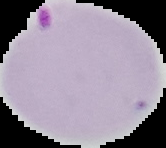
From a thin blood smear. The area outside the segmented cell region is set to black. Malaria status: parasitized. Image is 166×148 pixels.